Identify the cell.
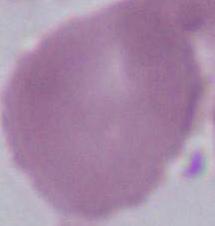

This is an erythrocyte.

Micrograph. 1000x magnification.